Classify this cell by malaria status.
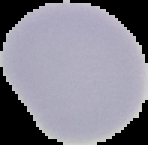
It is uninfected.

Summary:
  - Image type: segmented cell region with the area outside set to black
  - Preparation: thin blood film
  - Image size: 148×145 pixels